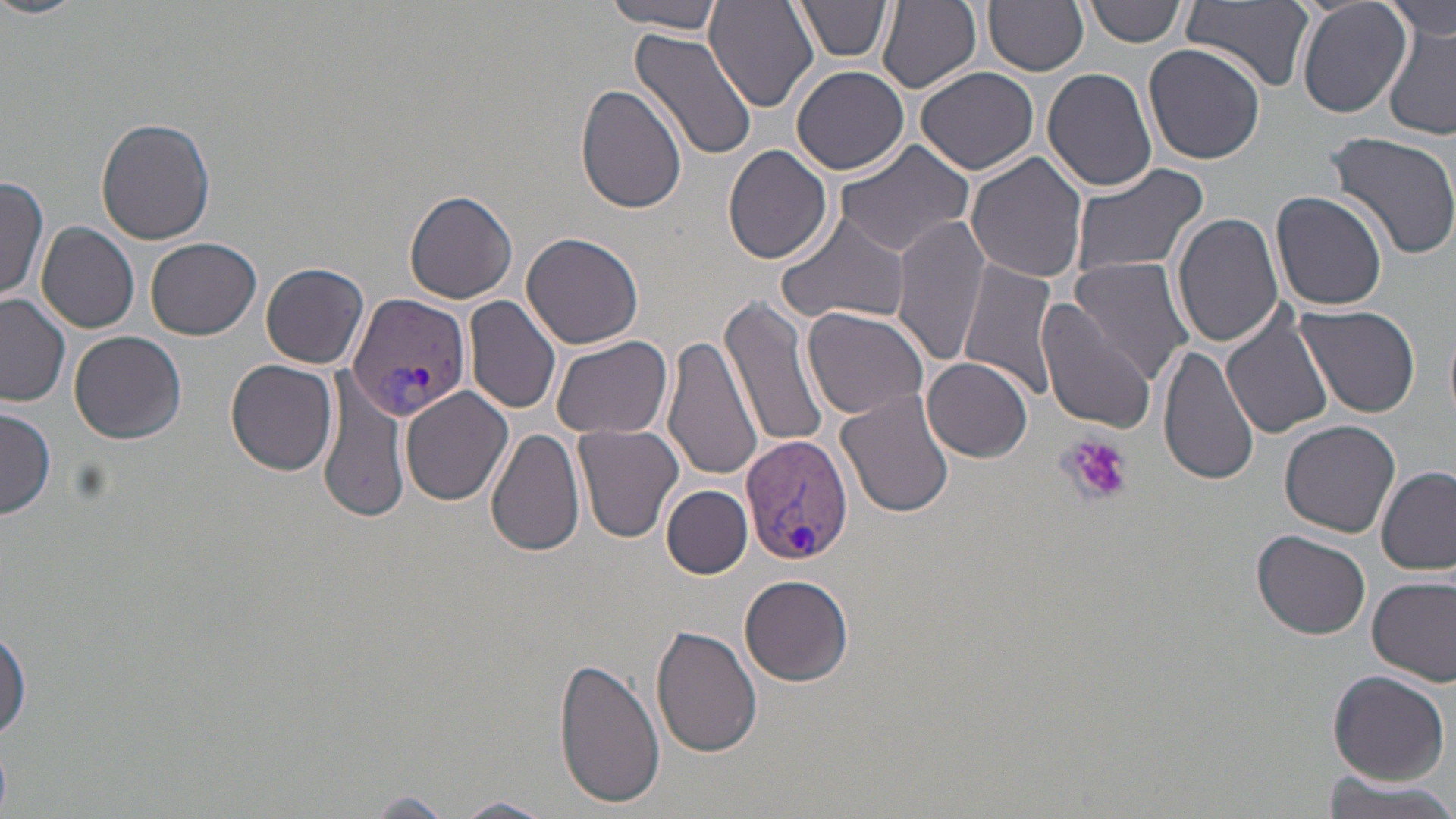

Summary:
  - Coordinate format: approximate bounding boxes as (x1,y1)-(x2,y2) corner pairs in pixels
  - Uninfected red blood cell locations: (0,0)-(84,22), (604,0)-(729,32), (878,0)-(981,93), (986,0)-(1088,76), (1294,0)-(1411,119), (1385,0)-(1455,42), (706,1)-(817,113), (793,1)-(895,62), (1085,1)-(1185,47), (1183,1)-(1315,92), (1383,25)-(1456,139), (629,29)-(759,161), (1144,43)-(1266,166), (791,65)-(910,174), (915,65)-(1039,175), (1042,67)-(1159,193), (575,84)-(688,216), (95,117)-(216,245), (1319,130)-(1456,260), (833,137)-(978,260), (723,143)-(832,264), (967,152)-(1088,284), (1067,160)-(1209,282), (0,176)-(49,304), (404,190)-(518,304), (1271,191)-(1390,312), (1172,210)-(1285,347), (774,213)-(912,326), (892,213)-(991,368), (36,220)-(139,332), (521,231)-(643,350), (147,237)-(261,340), (1068,256)-(1195,385), (957,258)-(1060,401), (261,261)-(369,369), (0,294)-(71,407), (719,294)-(831,454), (463,295)-(562,415), (1037,297)-(1153,432), (1294,303)-(1422,419), (1221,304)-(1338,439), (801,305)-(932,421), (70,329)-(186,444), (552,334)-(674,438), (664,335)-(762,483), (1157,338)-(1260,488), (923,356)-(1034,461), (227,359)-(340,475), (317,382)-(409,525), (401,386)-(513,506), (837,392)-(958,519), (0,403)-(56,521), (1280,417)-(1400,536), (572,423)-(686,545), (486,428)-(586,557), (1376,467)-(1455,576), (662,485)-(752,578), (1252,530)-(1371,640), (740,574)-(854,686), (1367,574)-(1456,685), (0,625)-(30,741), (650,625)-(761,758), (554,656)-(665,810), (1327,670)-(1448,784), (1319,774)-(1456,819), (360,793)-(457,817), (448,796)-(556,819)
  - Platelet locations: (1061,435)-(1132,505)
  - Plasmodium vivax-infected red blood cell locations: (345,292)-(472,422), (741,432)-(855,569)
  - Slide-level diagnosis: Plasmodium vivax
  - Modality: optical microscopy
  - Stain: May-Grünwald-Giemsa
  - Field of view: single
  - Magnification: 1000x
  - Preparation: thin blood smear
  - Image size: 1456×819 pixels